Report the malaria status of this cell.
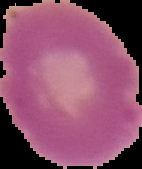
Uninfected.

preparation = thin blood smear
image size = 142×169 pixels
image type = cell region segmented out of the field of view; surrounding area masked to black